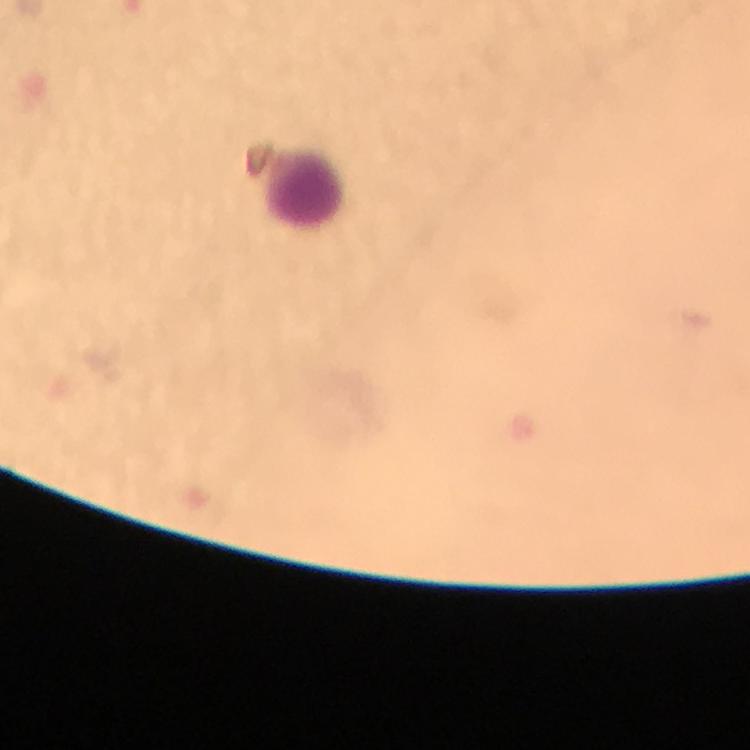

Approximate centers as [x, y] in pixels. Leukocyte locations: [302, 191]. Giemsa-stained preparation. Cropped region of a single field of view. Photographed through the microscope with a smartphone camera. Plasmodium parasites: none detected. Immersion oil applied. Image is 750×750 pixels. From a diagnostic examination for malaria. Thick blood film. 100x magnification.